Classify this cell by malaria status.
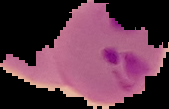

Parasitized.

Image is 169×109 pixels. From a thin blood smear. Segmented cell region on a black background.